Assess the morphology of the erythrocytes.
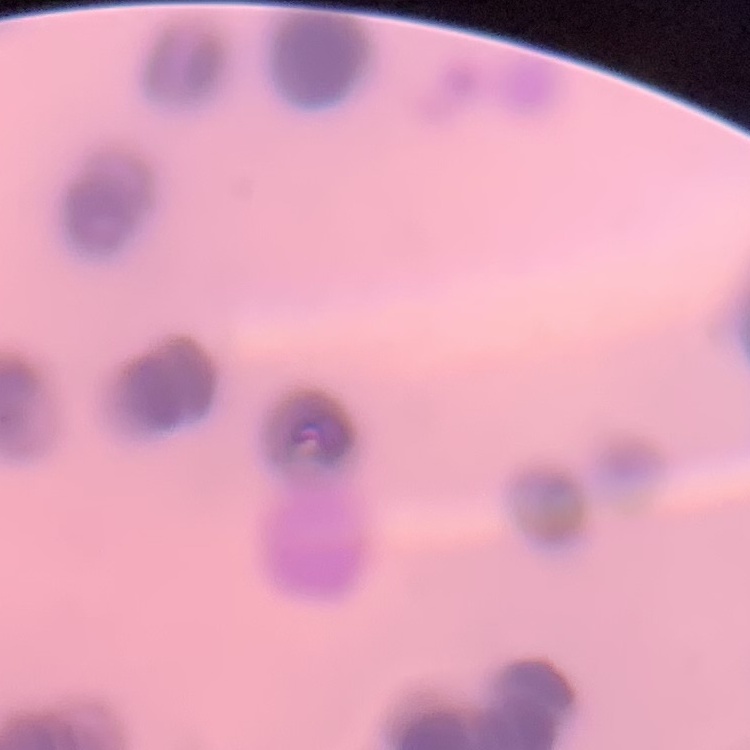
Rouleaux formation.

One tile cut from a larger photomicrograph. Thin blood smear. Field's or Giemsa stain.